Assess the morphology of the erythrocytes.
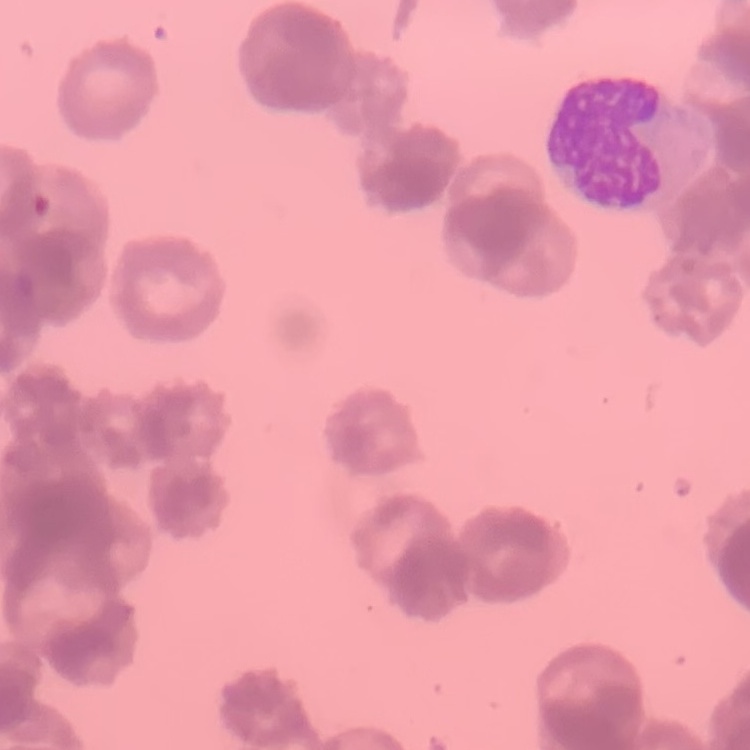
Rouleaux formation.

Square crop of a larger photomicrograph. Thin blood smear. Stained with either Field's or Giemsa.